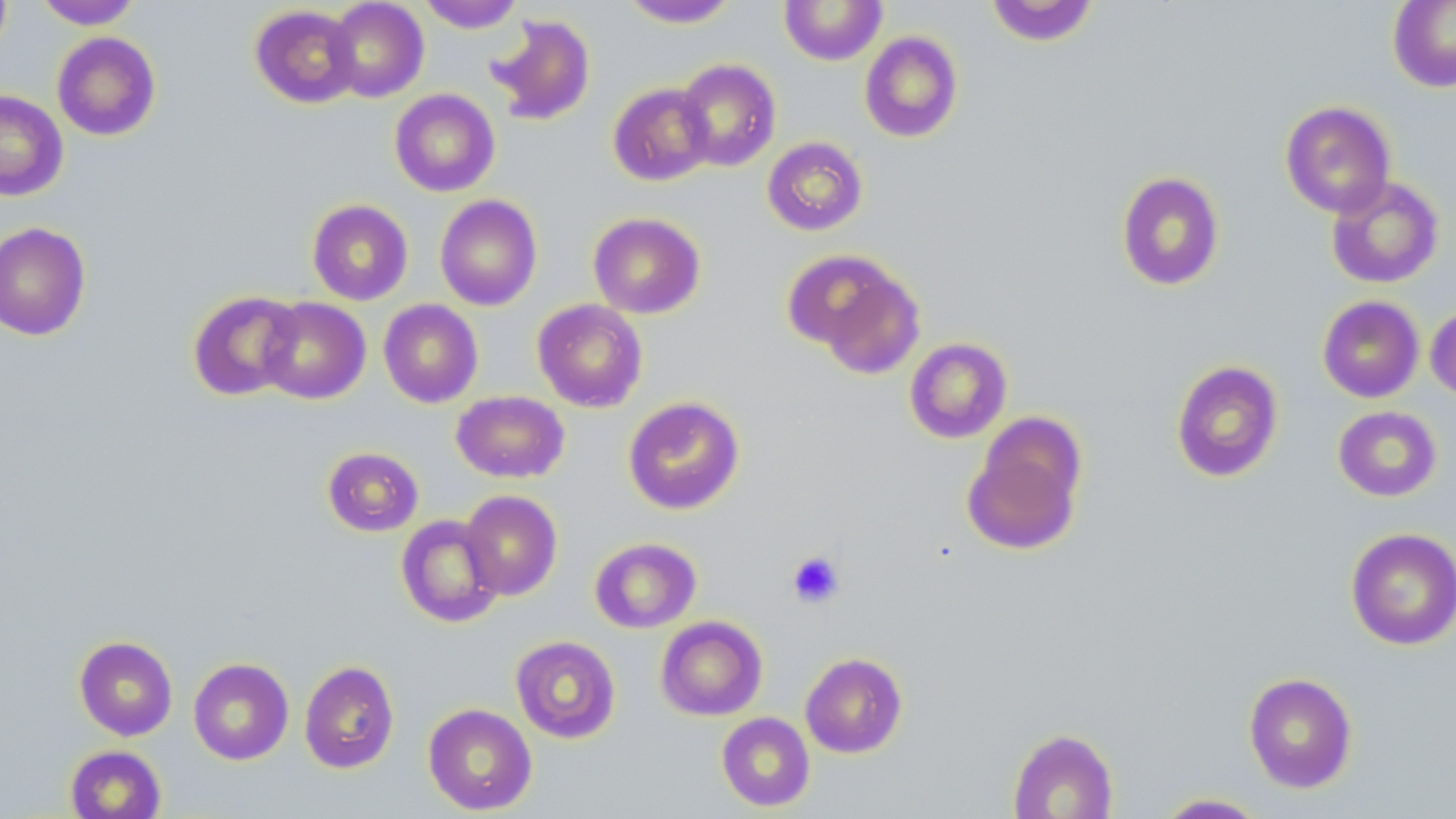

Approximate bounding boxes as (x1,y1)-(x2,y2) corner pairs in pixels. Uninfected red blood cell locations: (0,0)-(12,58), (33,0)-(144,29), (325,0)-(429,102), (417,0)-(525,33), (620,0)-(739,27), (780,0)-(886,65), (1388,0)-(1456,92), (985,1)-(1100,46), (249,4)-(361,108), (488,14)-(596,126), (859,31)-(964,143), (52,32)-(161,141), (675,58)-(781,172), (608,83)-(714,186), (389,88)-(500,197), (0,90)-(68,200), (1280,100)-(1396,217), (762,136)-(868,236), (1116,172)-(1224,291), (1326,175)-(1444,289), (434,195)-(542,311), (306,199)-(413,305), (588,212)-(706,319), (0,221)-(91,341), (789,250)-(926,374), (187,290)-(303,401), (1317,295)-(1424,402), (258,297)-(371,404), (532,298)-(648,412), (378,299)-(483,408), (1425,304)-(1456,402), (904,337)-(1013,443), (1170,360)-(1284,483), (451,391)-(569,483), (623,396)-(745,515), (1333,405)-(1442,501), (962,423)-(1086,556), (322,446)-(424,536), (460,490)-(562,600), (396,514)-(504,627), (1345,527)-(1456,650), (589,537)-(701,633), (655,616)-(767,721), (74,635)-(178,741), (511,635)-(621,743), (800,652)-(907,758), (188,657)-(294,765), (299,660)-(399,774), (1243,672)-(1358,793), (423,703)-(537,815), (716,712)-(815,812), (1007,728)-(1119,818), (64,744)-(167,819), (1152,793)-(1270,818). Platelet locations: (787,550)-(844,608). Slide-level diagnosis: negative for blood parasites. Image is 1456×819 pixels. May-Grünwald-Giemsa stain. Light microscopy. 1000x magnification. Thin blood smear. Single field of view.